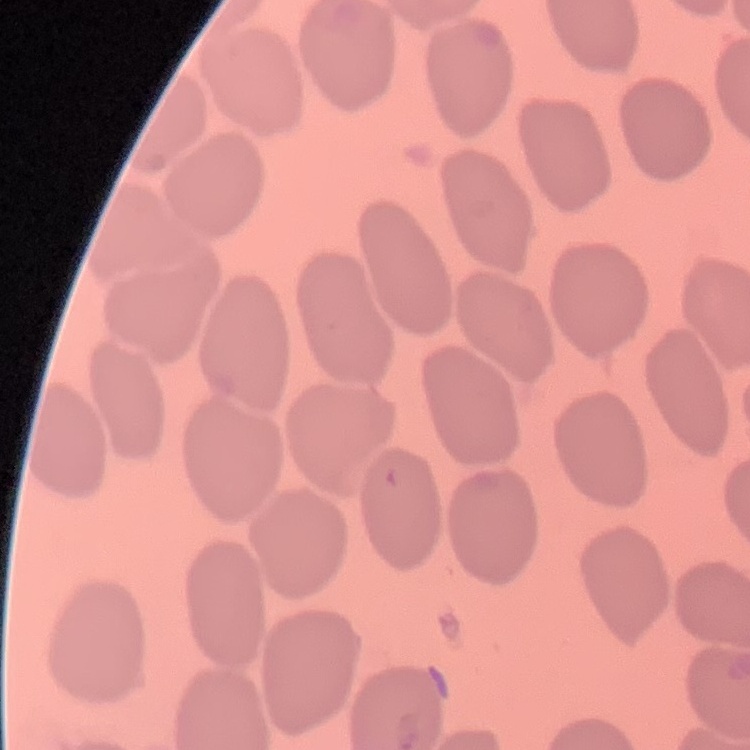

erythrocyte morphology = no rouleaux formation
stain = Field's or Giemsa
image type = one tile cut from a larger photomicrograph
preparation = thin blood smear